Assess this cell for malaria.
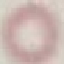
It is uninfected.

capture: smartphone camera at the microscope eyepiece
preparation: thin blood film
image_type: cell patch, automatically extracted from a larger field of view and resized to 64 × 64 pixels
stain: Giemsa